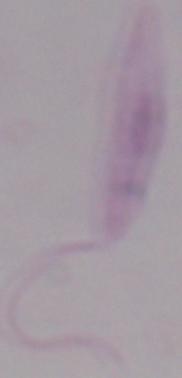
Summary:
  - Identification: Leishmania
  - Magnification: 1000x
  - Modality: micrograph